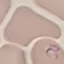
malaria status = parasitized
preparation = thin blood film
stain = Giemsa
image type = automatically extracted cell patch, resized to 64 × 64 pixels
capture = smartphone camera at the microscope eyepiece